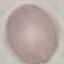

Summary:
  - Result: no malaria parasites detected
  - Stain: Giemsa
  - Image type: cell patch, automatically extracted from a larger field of view and resized to 64 × 64 pixels
  - Capture: smartphone through the microscope eyepiece
  - Preparation: thin smear